Locate every uninfected red blood cell.
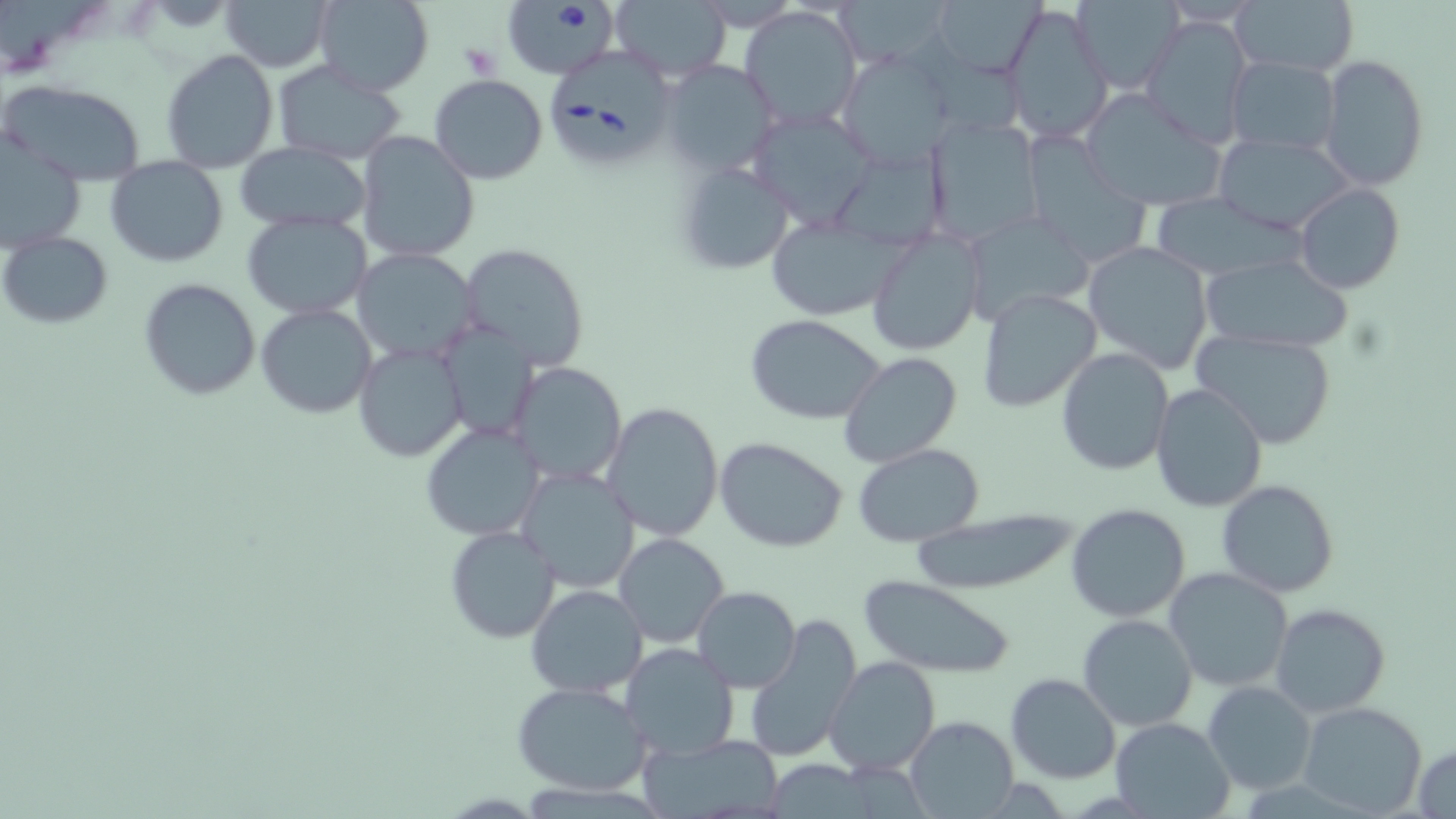

Approximate bounding boxes as named x1/y1/x2/y2 corners in pixels.
Uninfected red blood cells: (x1=221, y1=0, x2=332, y2=72), (x1=313, y1=0, x2=435, y2=96), (x1=834, y1=0, x2=951, y2=67), (x1=932, y1=0, x2=1044, y2=77), (x1=1071, y1=0, x2=1181, y2=90), (x1=1230, y1=1, x2=1358, y2=79), (x1=609, y1=2, x2=730, y2=79), (x1=1005, y1=3, x2=1114, y2=142), (x1=740, y1=5, x2=862, y2=129), (x1=1141, y1=14, x2=1253, y2=149), (x1=159, y1=48, x2=279, y2=174), (x1=837, y1=51, x2=954, y2=167), (x1=1226, y1=55, x2=1341, y2=155), (x1=1319, y1=55, x2=1429, y2=191), (x1=661, y1=60, x2=780, y2=177), (x1=270, y1=62, x2=407, y2=162), (x1=429, y1=74, x2=549, y2=185), (x1=2, y1=79, x2=147, y2=187), (x1=1078, y1=88, x2=1228, y2=213), (x1=926, y1=117, x2=1044, y2=244), (x1=356, y1=131, x2=480, y2=264), (x1=1020, y1=133, x2=1153, y2=268), (x1=1213, y1=133, x2=1355, y2=235), (x1=0, y1=139, x2=86, y2=253), (x1=234, y1=143, x2=371, y2=231), (x1=106, y1=157, x2=228, y2=267), (x1=673, y1=160, x2=796, y2=275), (x1=1295, y1=183, x2=1404, y2=296), (x1=1149, y1=194, x2=1305, y2=279), (x1=243, y1=211, x2=371, y2=317), (x1=962, y1=212, x2=1097, y2=326), (x1=764, y1=215, x2=908, y2=320), (x1=866, y1=226, x2=986, y2=355), (x1=2, y1=232, x2=113, y2=330), (x1=1083, y1=239, x2=1215, y2=375), (x1=459, y1=243, x2=590, y2=374), (x1=353, y1=249, x2=478, y2=365), (x1=1200, y1=254, x2=1350, y2=353), (x1=139, y1=277, x2=261, y2=401), (x1=976, y1=286, x2=1104, y2=414), (x1=255, y1=303, x2=376, y2=419), (x1=744, y1=314, x2=888, y2=425), (x1=440, y1=321, x2=537, y2=441), (x1=1194, y1=327, x2=1338, y2=450), (x1=354, y1=344, x2=466, y2=461), (x1=1056, y1=346, x2=1174, y2=476), (x1=839, y1=353, x2=963, y2=469), (x1=510, y1=362, x2=627, y2=486), (x1=1152, y1=382, x2=1269, y2=513), (x1=602, y1=401, x2=725, y2=540), (x1=421, y1=424, x2=545, y2=541), (x1=716, y1=436, x2=848, y2=553), (x1=852, y1=444, x2=987, y2=545), (x1=516, y1=466, x2=641, y2=593), (x1=1215, y1=479, x2=1339, y2=598), (x1=1064, y1=504, x2=1191, y2=623), (x1=907, y1=510, x2=1079, y2=596), (x1=444, y1=524, x2=560, y2=643), (x1=614, y1=532, x2=730, y2=647), (x1=1163, y1=566, x2=1294, y2=692), (x1=860, y1=576, x2=1014, y2=676), (x1=525, y1=584, x2=649, y2=699), (x1=693, y1=586, x2=802, y2=694), (x1=1270, y1=603, x2=1393, y2=717), (x1=745, y1=613, x2=863, y2=764), (x1=1078, y1=614, x2=1197, y2=733), (x1=621, y1=642, x2=740, y2=760), (x1=824, y1=655, x2=940, y2=774), (x1=1005, y1=671, x2=1122, y2=784), (x1=513, y1=680, x2=651, y2=798), (x1=1202, y1=680, x2=1316, y2=796), (x1=1298, y1=701, x2=1428, y2=818), (x1=903, y1=715, x2=1018, y2=818), (x1=1109, y1=716, x2=1235, y2=817), (x1=642, y1=733, x2=782, y2=817), (x1=1414, y1=742, x2=1456, y2=818).

Summary:
  - Platelet locations: (x1=458, y1=44, x2=500, y2=81)
  - Babesia divergens-infected red blood cell locations: (x1=503, y1=3, x2=616, y2=80), (x1=548, y1=55, x2=680, y2=174)
  - Slide-level diagnosis: Babesia divergens
  - Modality: light microscopy
  - Field of view: single
  - Preparation: thin blood smear
  - Magnification: 1000x
  - Image size: 1456×819 pixels
  - Stain: May-Grünwald-Giemsa